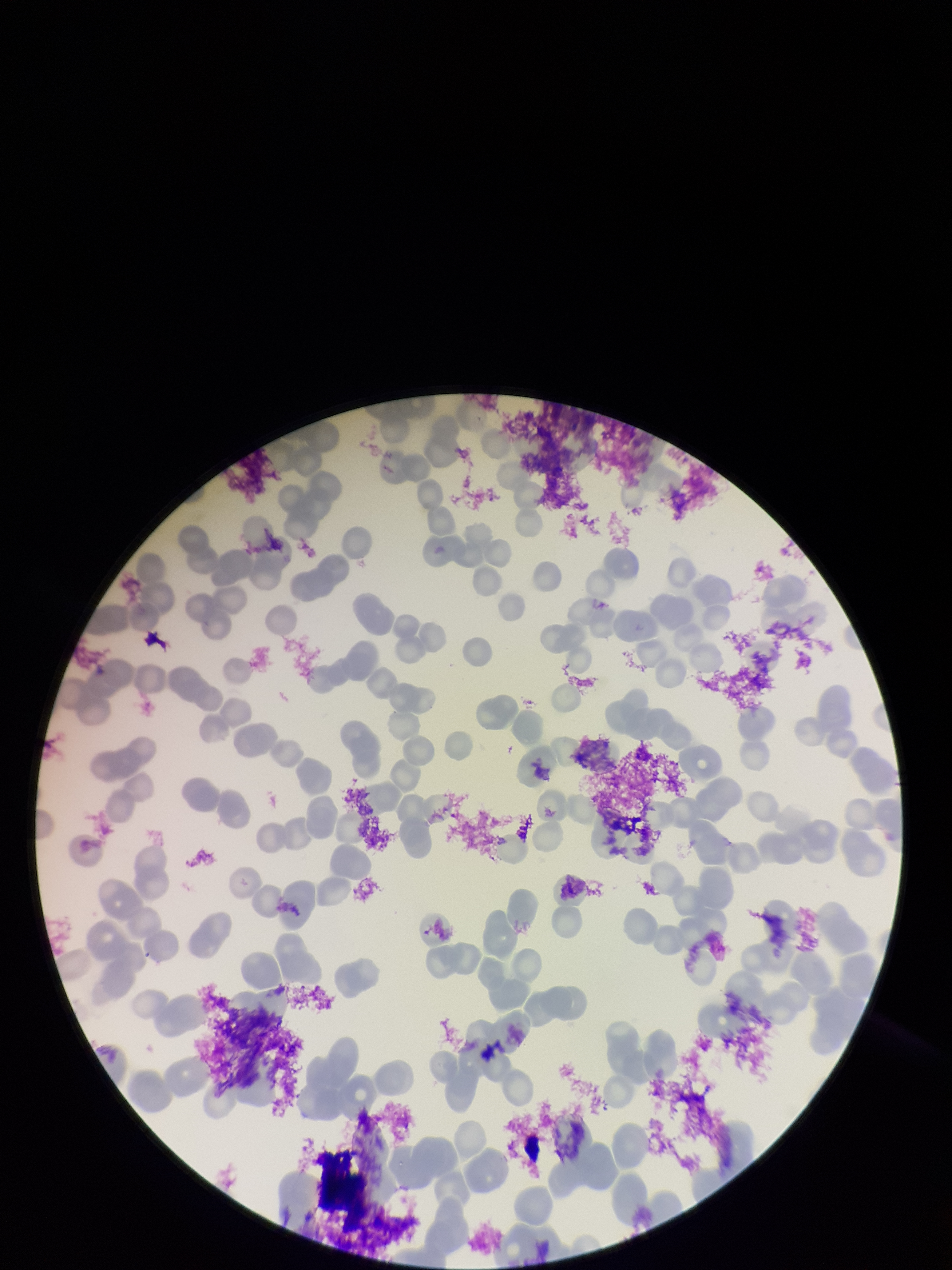
stain = Giemsa
parasitized red blood cell count = 0
field of view = one from this slide
parasitized red blood cells = none identified
image size = 952×1270 pixels
red blood cell count = 139
patient malaria status = infected
capture = smartphone photograph through the microscope eyepiece
species reported for this patient = Plasmodium falciparum
preparation = thin